Assess the morphology of the red blood cells.
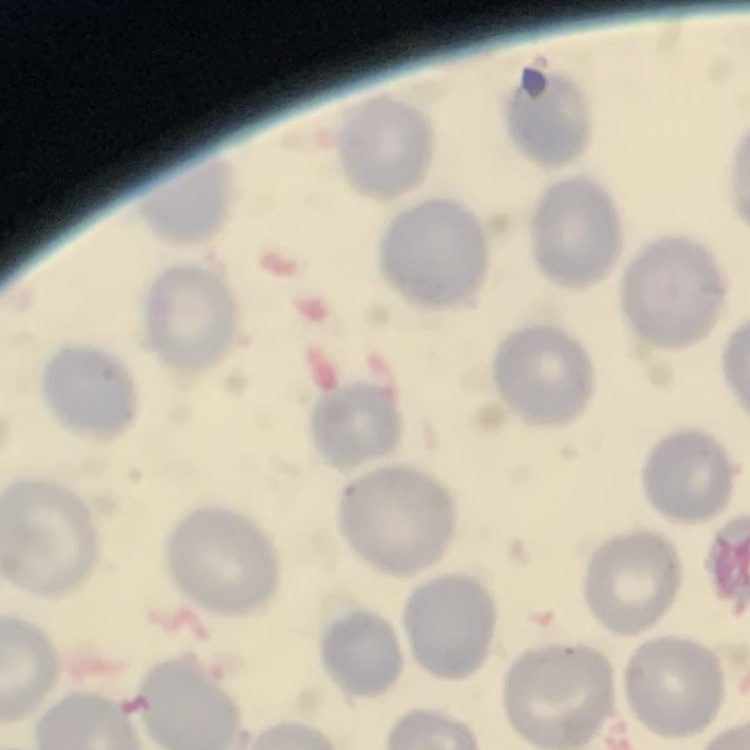

They show no rouleaux formation.

{
  "preparation": "thin peripheral smear",
  "stain": "Field's or Giemsa",
  "image_type": "square crop of a larger photomicrograph"
}